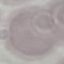 Malaria status: uninfected. Thin smear of blood. Automatically extracted cell patch, resized to 64 × 64 pixels. Photographed with a smartphone camera at the microscope eyepiece. Giemsa-stained preparation.